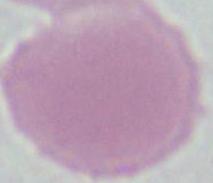
magnification: 1000x
modality: micrograph
identification: erythrocyte